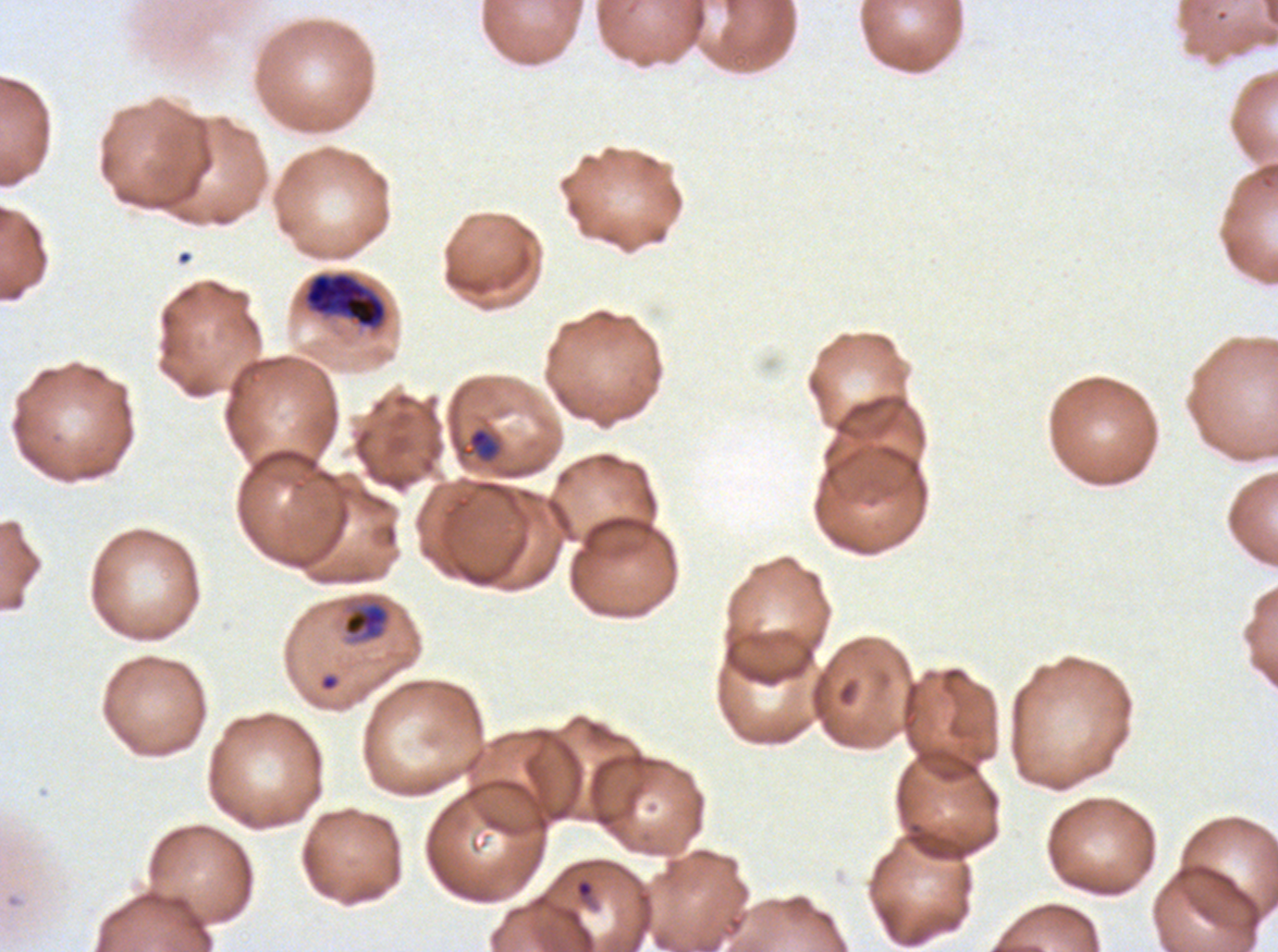
Approximate bounding boxes as (x1, y1, x2, y2) in pixels. Object labeled both late-ring/early-trophozoite and late trophozoite by the source: (341, 597, 392, 644). Late-ring/early-trophozoite locations: (461, 426, 502, 464). Early schizont locations: (304, 273, 387, 328). Ring locations: (575, 879, 594, 898). Thin blood film. A sub-image separated from a larger composite. Image is 1278×952 pixels. Life-cycle stages observed: ring, late-ring/early-trophozoite, early schizont. P. falciparum cultured ex vivo for 24 to 48 hours, from a patient in The Gambia. Giemsa stain.